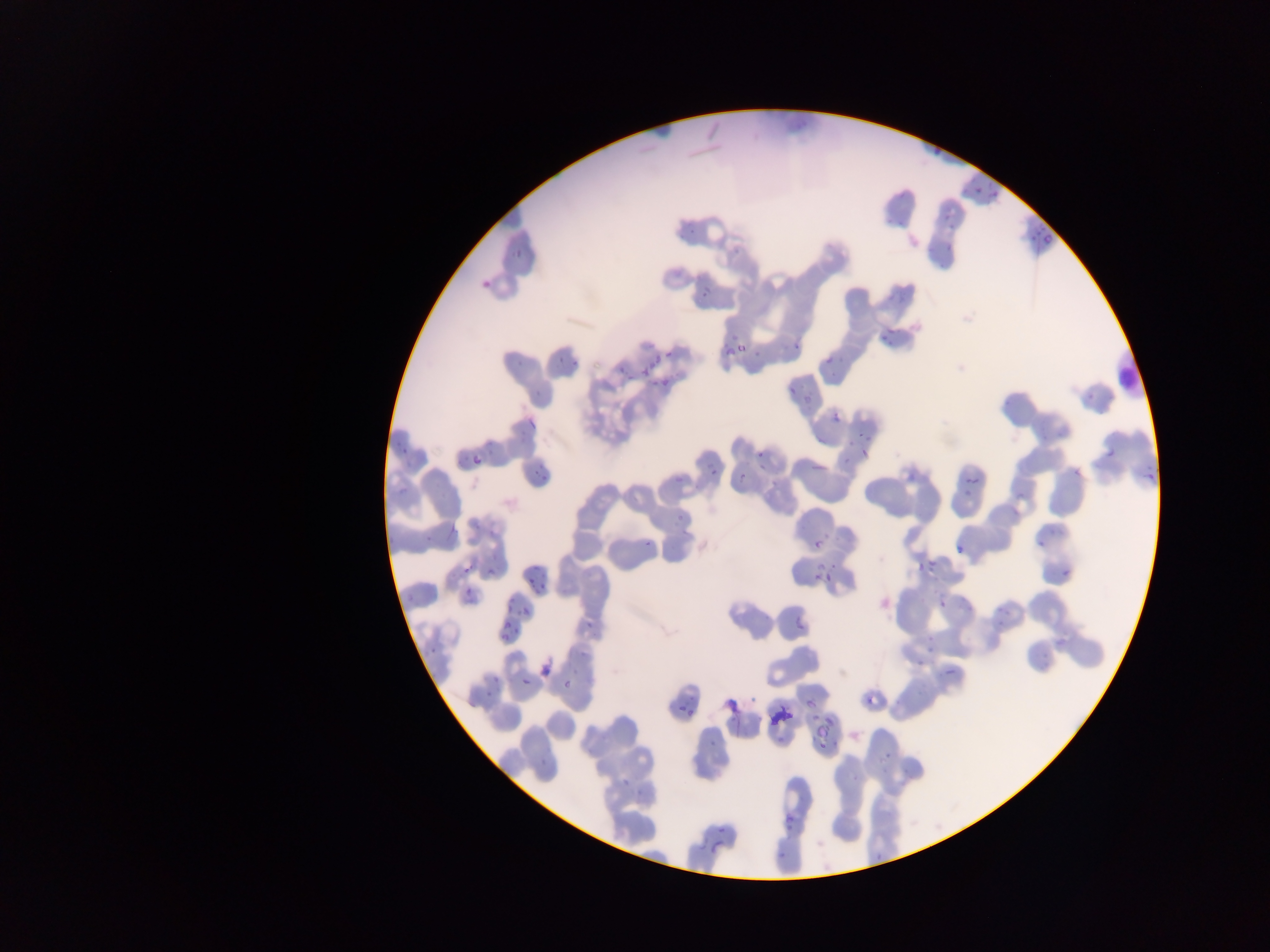
Approximate bounding boxes as {left, top, right, bottom} in pixels. Malaria parasite locations: {934, 144, 943, 155}, {969, 184, 983, 195}, {988, 189, 998, 200}, {939, 211, 949, 221}, {681, 221, 703, 236}, {1027, 227, 1051, 244}, {938, 242, 954, 254}, {509, 247, 531, 264}, {478, 272, 498, 291}, {701, 287, 712, 299}, {888, 292, 907, 308}, {874, 327, 896, 349}, {732, 334, 751, 361}, {790, 341, 799, 352}, {751, 343, 768, 362}, {723, 344, 733, 357}, {551, 351, 570, 368}, {665, 351, 674, 359}, {647, 354, 660, 368}, {825, 357, 833, 366}, {615, 367, 631, 378}, {640, 367, 652, 380}, {641, 368, 649, 376}, {662, 377, 674, 392}, {786, 383, 800, 394}, {1080, 387, 1107, 401}, {801, 397, 808, 409}, {831, 412, 841, 422}, {527, 418, 537, 429}, {857, 426, 870, 445}, {815, 431, 836, 448}, {396, 440, 414, 459}, {860, 446, 871, 459}, {1107, 448, 1116, 459}, {756, 450, 765, 459}, {472, 456, 482, 465}, {810, 461, 830, 478}, {1137, 461, 1159, 490}, {1067, 464, 1080, 478}, {709, 466, 716, 476}, {902, 467, 916, 482}, {536, 470, 552, 481}, {963, 471, 982, 488}, {738, 472, 745, 480}, {394, 476, 414, 496}, {1012, 482, 1029, 497}, {960, 484, 973, 501}, {670, 512, 692, 526}, {1031, 528, 1050, 549}, {423, 530, 441, 543}, {640, 539, 655, 546}, {812, 539, 821, 548}, {952, 545, 966, 559}, {914, 553, 938, 572}, {825, 561, 849, 580}, {461, 563, 475, 576}, {483, 565, 495, 576}, {1059, 567, 1070, 576}, {525, 572, 535, 583}, {812, 572, 820, 580}, {462, 587, 469, 598}, {506, 598, 517, 610}, {937, 599, 949, 610}, {520, 607, 530, 617}, {505, 618, 514, 629}, {796, 621, 805, 630}, {499, 632, 508, 641}, {425, 642, 440, 655}, {925, 647, 934, 657}, {914, 651, 926, 668}, {939, 664, 956, 676}, {521, 677, 531, 686}, {563, 680, 571, 690}, {861, 682, 890, 710}, {487, 683, 501, 694}, {804, 693, 821, 714}, {683, 707, 693, 717}, {784, 711, 794, 722}, {807, 726, 841, 751}, {710, 739, 723, 748}, {881, 755, 894, 765}, {783, 814, 795, 828}, {716, 825, 727, 834}, {709, 828, 726, 850}, {710, 842, 721, 854}, {777, 847, 789, 861}. Photographed through a microscope with a mobile-phone camera. Thin blood smear. Image is 1270×952 pixels. Sample from Ghana. One field of view.